Locate every Plasmodium parasite.
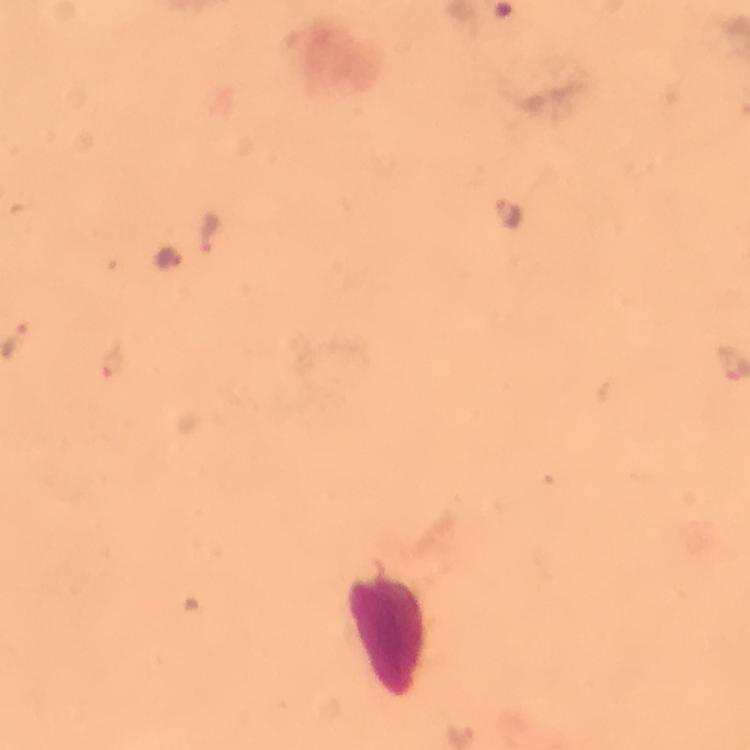
Approximate centers as [x, y] in pixels.
Plasmodium parasites: [509, 212], [209, 232], [170, 256], [13, 337], [114, 360].

{
  "immersion_oil": "used",
  "image_size": "750×750 pixels",
  "magnification": "100x",
  "context": "from a malaria diagnostic workup",
  "capture": "smartphone camera through the microscope",
  "stain": "Giemsa",
  "preparation": "thick blood film",
  "cropped_from": "one field of view"
}